Assess this cell for malaria.
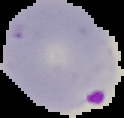

Parasitized.

From a thin blood film. Segmented cell region on a black background. Image is 124×118 pixels.